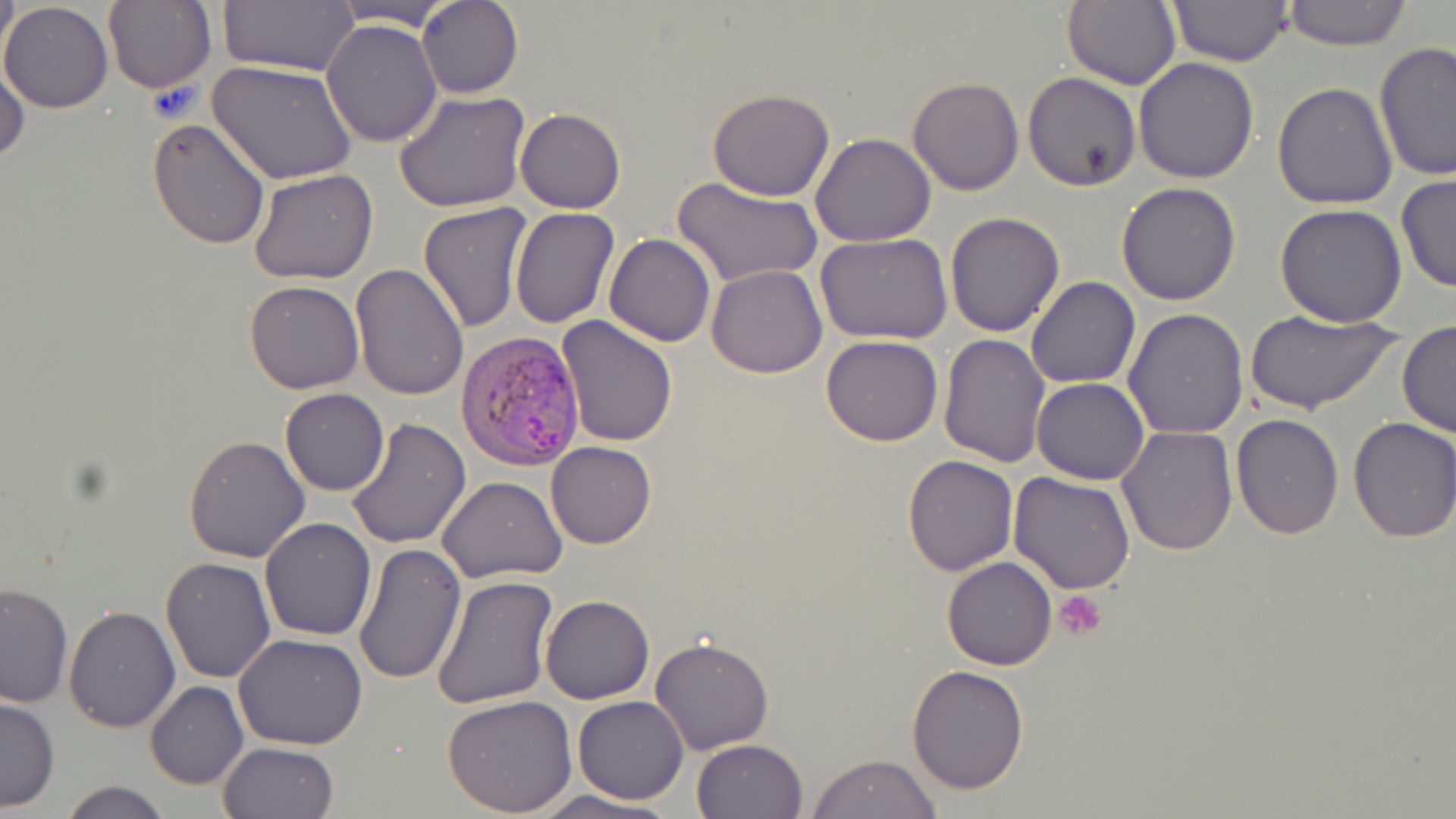

Approximate bounding boxes as named x1/y1/x2/y2 corners in pixels. Uninfected red blood cell locations: (x1=0, y1=0, x2=19, y2=68), (x1=326, y1=0, x2=459, y2=29), (x1=417, y1=0, x2=523, y2=99), (x1=1063, y1=0, x2=1182, y2=92), (x1=1167, y1=0, x2=1294, y2=67), (x1=1278, y1=0, x2=1414, y2=50), (x1=103, y1=1, x2=215, y2=93), (x1=215, y1=1, x2=359, y2=75), (x1=0, y1=2, x2=114, y2=113), (x1=322, y1=19, x2=442, y2=146), (x1=1374, y1=42, x2=1455, y2=180), (x1=1, y1=50, x2=29, y2=166), (x1=1133, y1=57, x2=1260, y2=185), (x1=207, y1=59, x2=356, y2=187), (x1=1023, y1=72, x2=1141, y2=191), (x1=907, y1=76, x2=1024, y2=197), (x1=1272, y1=82, x2=1400, y2=210), (x1=707, y1=88, x2=835, y2=202), (x1=394, y1=89, x2=529, y2=211), (x1=515, y1=107, x2=625, y2=214), (x1=146, y1=119, x2=271, y2=249), (x1=811, y1=131, x2=935, y2=247), (x1=249, y1=168, x2=378, y2=284), (x1=1395, y1=174, x2=1456, y2=293), (x1=674, y1=176, x2=821, y2=287), (x1=1116, y1=181, x2=1242, y2=305), (x1=417, y1=202, x2=534, y2=333), (x1=1274, y1=204, x2=1407, y2=327), (x1=510, y1=208, x2=619, y2=328), (x1=945, y1=212, x2=1067, y2=337), (x1=815, y1=232, x2=955, y2=346), (x1=605, y1=233, x2=715, y2=347), (x1=350, y1=263, x2=469, y2=399), (x1=707, y1=265, x2=826, y2=378), (x1=1026, y1=276, x2=1140, y2=388), (x1=243, y1=279, x2=364, y2=394), (x1=1123, y1=308, x2=1249, y2=438), (x1=1246, y1=308, x2=1398, y2=416), (x1=555, y1=315, x2=677, y2=447), (x1=1397, y1=323, x2=1456, y2=438), (x1=937, y1=333, x2=1049, y2=468), (x1=820, y1=335, x2=943, y2=446), (x1=1032, y1=377, x2=1149, y2=484), (x1=280, y1=388, x2=389, y2=495), (x1=1231, y1=414, x2=1343, y2=539), (x1=1347, y1=418, x2=1456, y2=542), (x1=346, y1=419, x2=471, y2=549), (x1=1117, y1=425, x2=1237, y2=557), (x1=183, y1=433, x2=311, y2=562), (x1=546, y1=441, x2=657, y2=548), (x1=901, y1=453, x2=1019, y2=575), (x1=1008, y1=471, x2=1137, y2=593), (x1=437, y1=475, x2=567, y2=582), (x1=259, y1=518, x2=376, y2=642), (x1=352, y1=543, x2=466, y2=687), (x1=160, y1=555, x2=276, y2=684), (x1=942, y1=557, x2=1057, y2=670), (x1=431, y1=574, x2=560, y2=712), (x1=0, y1=582, x2=73, y2=708), (x1=539, y1=595, x2=655, y2=703), (x1=63, y1=606, x2=180, y2=732), (x1=233, y1=632, x2=368, y2=750), (x1=650, y1=637, x2=774, y2=754), (x1=906, y1=664, x2=1030, y2=795), (x1=144, y1=682, x2=248, y2=788), (x1=442, y1=694, x2=577, y2=816), (x1=571, y1=696, x2=690, y2=803), (x1=0, y1=697, x2=59, y2=813), (x1=691, y1=739, x2=807, y2=819), (x1=218, y1=741, x2=340, y2=819), (x1=808, y1=754, x2=941, y2=819), (x1=58, y1=780, x2=173, y2=819), (x1=530, y1=790, x2=677, y2=819). Plasmodium vivax-infected red blood cell locations: (x1=454, y1=329, x2=588, y2=469). Platelet locations: (x1=1055, y1=590, x2=1107, y2=641). Slide-level diagnosis: Plasmodium vivax. Image is 1456×819 pixels. May-Grünwald-Giemsa stain. Thin blood smear. Captured at 1000x magnification. Optical microscopy. One field of a larger specimen.